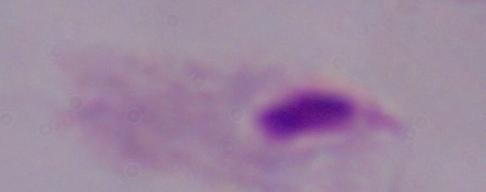

{
  "magnification": "1000x",
  "identification": "trichomonad",
  "modality": "photomicrograph"
}